State which parasite is depicted.
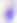

Toxoplasma gondii.

Summary:
  - Modality: photomicrograph
  - Magnification: 400x